Classify this cell by malaria status.
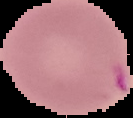

Parasitized.

preparation: thin blood smear
image_type: segmented cell region with the area outside set to black
image_size: 133×118 pixels